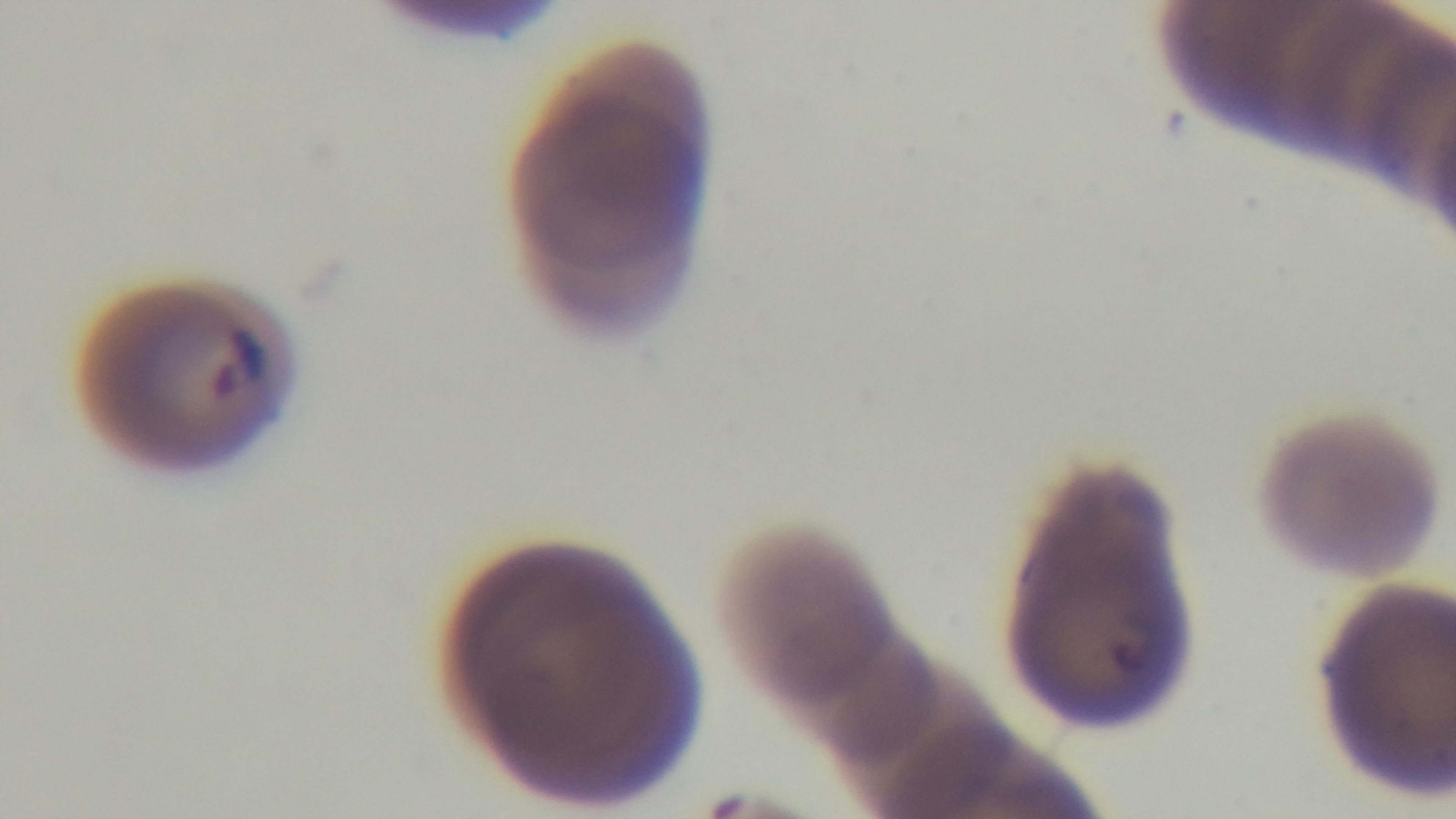

objective = 100x oil immersion
malaria status = positive
preparation = thin blood film
capture = mounted 4K digital camera
field of view = one from the slide
modality = light microscopy
stain = Giemsa